Outline each Plasmodium falciparum-infected red blood cell.
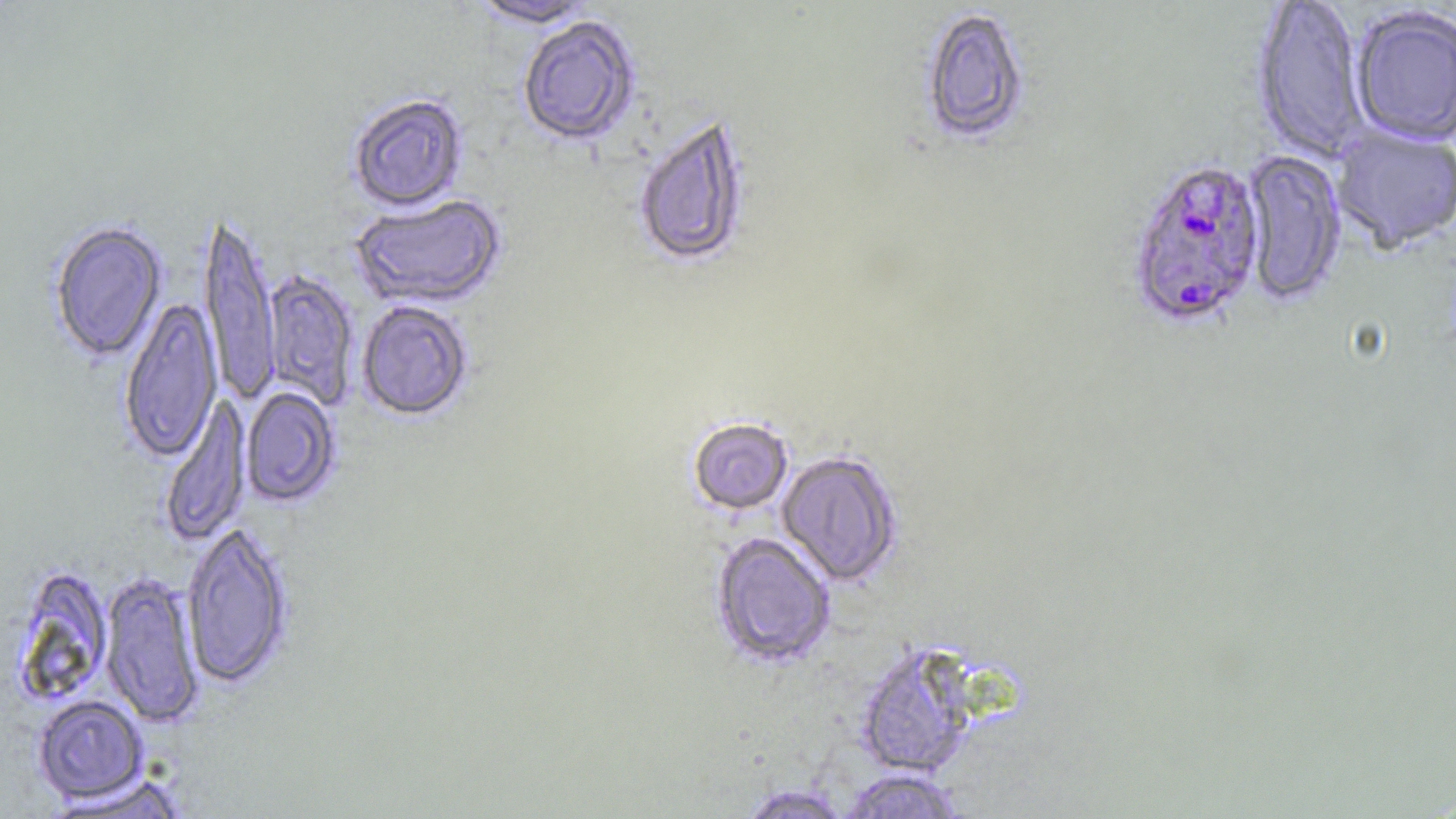

Approximate bounding boxes as named x1/y1/x2/y2 corners in pixels.
Plasmodium falciparum-infected red blood cells: (x1=1125, y1=159, x2=1267, y2=333).

Summary:
  - Uninfected red blood cell locations: (x1=468, y1=0, x2=598, y2=29), (x1=1249, y1=0, x2=1369, y2=165), (x1=919, y1=7, x2=1031, y2=148), (x1=1350, y1=8, x2=1456, y2=148), (x1=517, y1=17, x2=640, y2=147), (x1=348, y1=93, x2=468, y2=213), (x1=632, y1=116, x2=752, y2=270), (x1=1331, y1=126, x2=1456, y2=255), (x1=1240, y1=149, x2=1347, y2=307), (x1=350, y1=195, x2=506, y2=309), (x1=199, y1=212, x2=281, y2=404), (x1=48, y1=221, x2=167, y2=363), (x1=261, y1=270, x2=359, y2=410), (x1=119, y1=297, x2=222, y2=462), (x1=357, y1=300, x2=473, y2=421), (x1=240, y1=387, x2=341, y2=507), (x1=160, y1=397, x2=252, y2=546), (x1=688, y1=418, x2=793, y2=515), (x1=776, y1=451, x2=903, y2=588), (x1=180, y1=524, x2=294, y2=689), (x1=711, y1=532, x2=836, y2=669), (x1=9, y1=565, x2=114, y2=707), (x1=98, y1=571, x2=205, y2=727), (x1=854, y1=644, x2=979, y2=778), (x1=33, y1=695, x2=148, y2=804), (x1=837, y1=768, x2=966, y2=818), (x1=47, y1=774, x2=190, y2=817), (x1=736, y1=784, x2=853, y2=818)
  - Slide-level diagnosis: Plasmodium falciparum
  - Stain: May-Grünwald-Giemsa
  - Modality: optical microscopy
  - Image size: 1456×819 pixels
  - Field of view: one of a larger specimen
  - Preparation: thin blood film
  - Magnification: 1000x